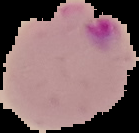
malaria status = parasitized
image type = segmented cell region on a black background
preparation = thin blood film
image size = 139×133 pixels